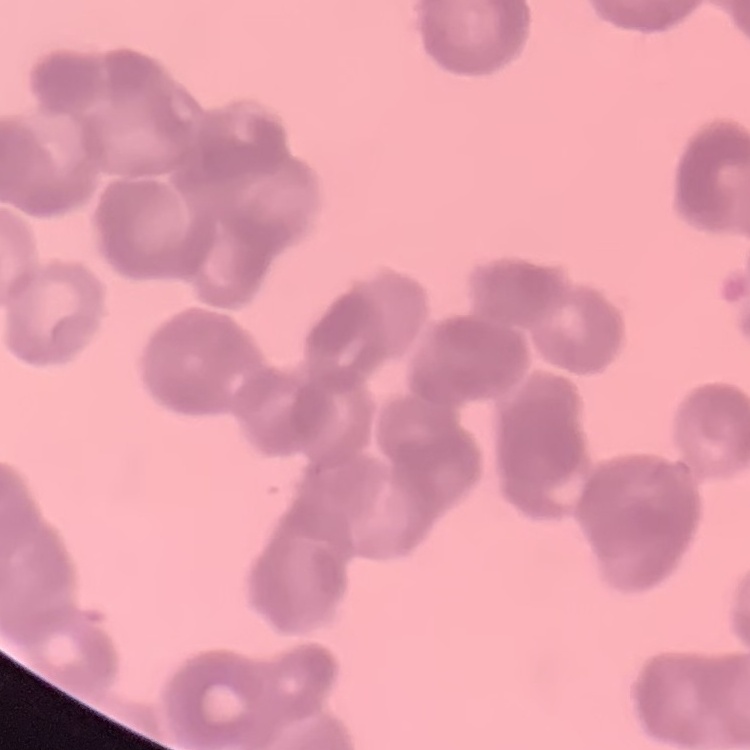
erythrocyte morphology = rouleaux formation
preparation = thin blood film
stain = Field's or Giemsa
image type = square crop of a larger photomicrograph